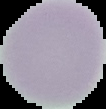

Summary:
  - Image type: segmented cell region on a black background
  - Result: negative for malaria parasites
  - Image size: 106×109 pixels
  - Preparation: thin blood film